Locate every blood parasite and identify its species.
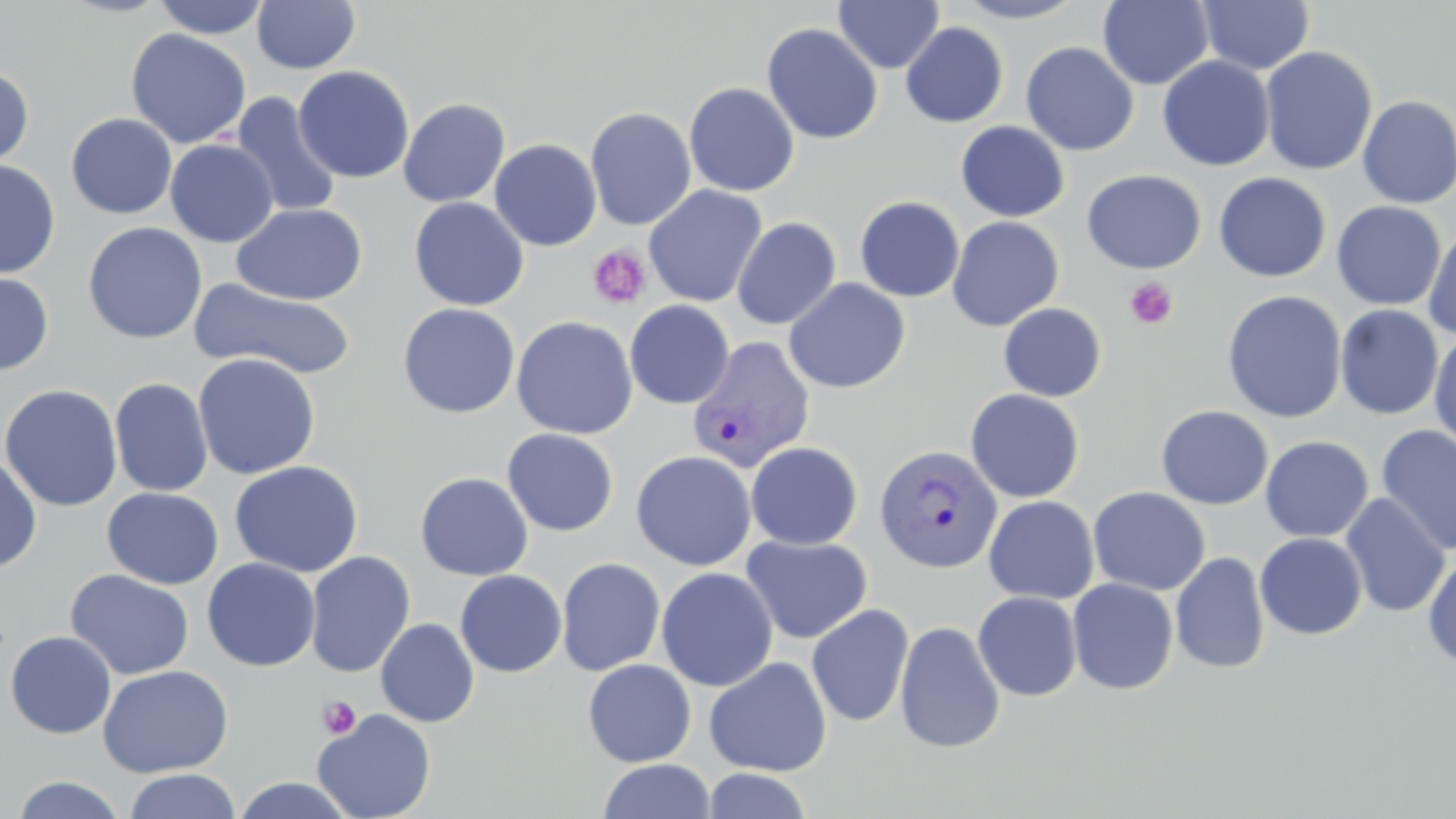

Approximate bounding boxes as (x1, y1, x2, y2) in pixels.
Plasmodium vivax-infected red blood cells: (687, 336, 816, 473), (873, 444, 1002, 573).
No Plasmodium falciparum, Plasmodium ovale, Plasmodium malariae, Babesia divergens, or Trypanosoma brucei observed.

Summary:
  - Platelet locations: (588, 244, 652, 309), (1124, 276, 1178, 330), (317, 696, 361, 740)
  - Uninfected red blood cell locations: (151, 0, 271, 39), (834, 0, 944, 73), (951, 0, 1088, 23), (1197, 0, 1315, 75), (251, 1, 361, 74), (1098, 1, 1214, 89), (761, 22, 883, 145), (900, 22, 1008, 128), (125, 28, 252, 149), (1020, 42, 1139, 156), (1259, 45, 1378, 176), (1157, 55, 1275, 171), (0, 65, 34, 172), (293, 65, 415, 184), (683, 82, 800, 196), (230, 92, 342, 219), (1356, 95, 1456, 209), (397, 97, 510, 207), (585, 106, 697, 231), (66, 113, 177, 219), (955, 121, 1070, 222), (165, 139, 278, 247), (489, 139, 602, 251), (0, 159, 60, 279), (1082, 169, 1206, 274), (1214, 172, 1332, 282), (643, 185, 767, 307), (854, 196, 965, 302), (408, 197, 529, 310), (1331, 201, 1446, 310), (231, 203, 368, 305), (731, 216, 842, 329), (947, 216, 1064, 331), (82, 222, 207, 344), (1422, 222, 1456, 342), (0, 269, 54, 376), (784, 278, 910, 394), (192, 279, 358, 380), (1222, 290, 1347, 423), (625, 300, 734, 408), (998, 302, 1107, 402), (397, 303, 520, 418), (1334, 304, 1443, 419), (511, 315, 638, 439), (1429, 331, 1456, 454), (193, 353, 321, 480), (109, 378, 213, 497), (0, 384, 123, 511), (965, 389, 1085, 502), (1155, 405, 1273, 510), (1375, 425, 1456, 556), (501, 428, 618, 536), (1260, 436, 1373, 542), (746, 441, 863, 550), (631, 450, 756, 571), (0, 452, 42, 574), (229, 460, 364, 577), (415, 472, 534, 581), (1088, 486, 1210, 596), (102, 488, 223, 589), (1339, 493, 1452, 618), (984, 495, 1098, 604), (1255, 532, 1367, 640), (740, 534, 873, 644), (1422, 549, 1456, 673), (305, 551, 415, 678), (1170, 552, 1270, 674), (556, 557, 666, 677), (202, 558, 320, 672), (655, 566, 778, 692), (65, 569, 194, 680), (455, 569, 567, 677), (1067, 578, 1179, 695), (972, 591, 1083, 701), (806, 603, 914, 727), (375, 618, 479, 727), (895, 620, 1006, 754), (5, 631, 117, 739), (703, 657, 832, 776), (582, 659, 697, 767), (98, 665, 233, 778), (312, 708, 437, 819), (597, 759, 716, 819), (702, 768, 813, 819), (124, 769, 241, 819), (11, 775, 128, 818), (231, 777, 358, 818)
  - Slide-level diagnosis: Plasmodium vivax
  - Stain: May-Grünwald-Giemsa
  - Preparation: thin blood smear
  - Image size: 1456×819 pixels
  - Magnification: 1000x
  - Modality: light microscopy
  - Field of view: single